Locate every Plasmodium parasite.
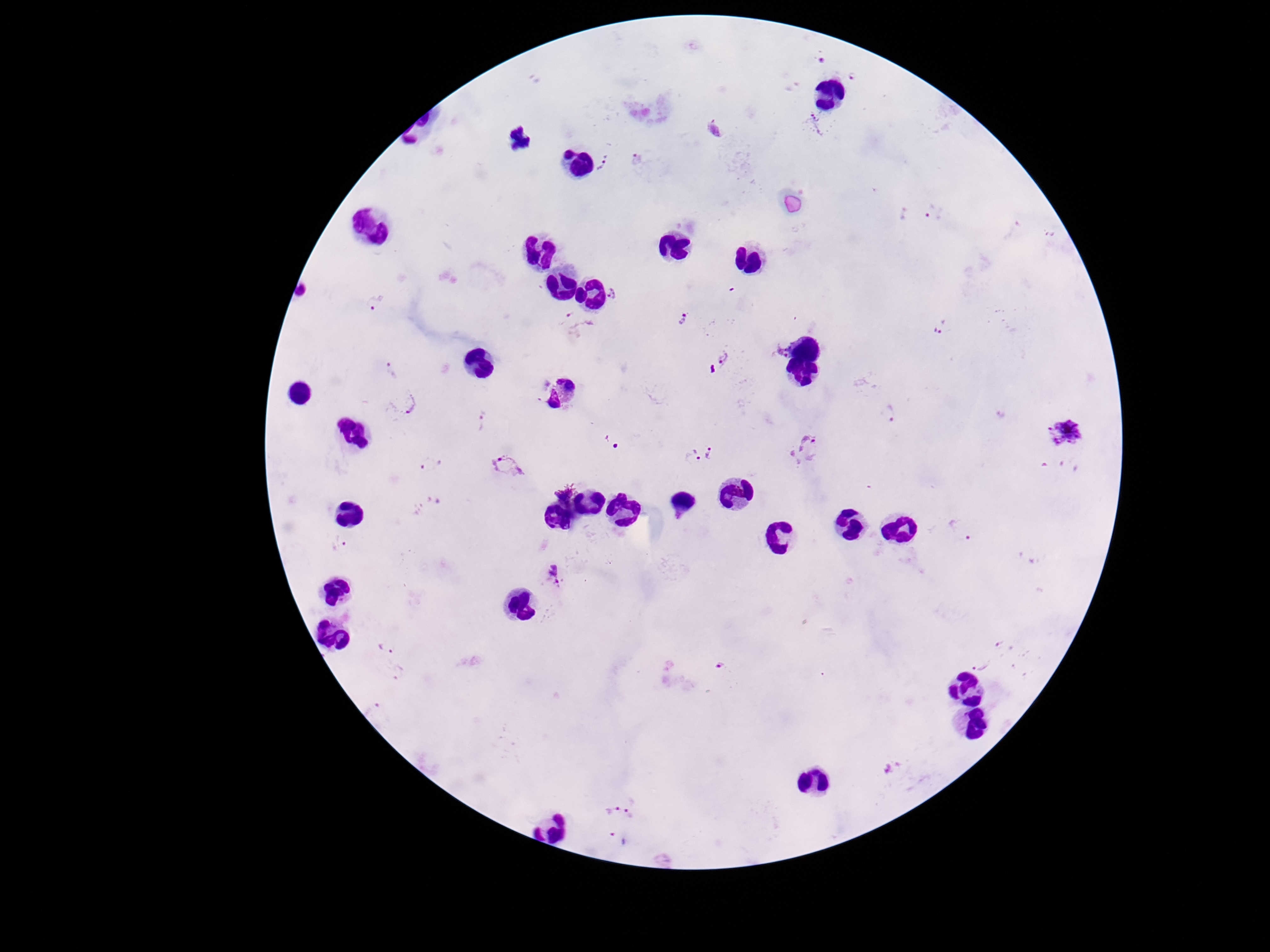

Approximate object centers, in pixels from the top-left corner.
Plasmodium parasites: (x=822, y=62), (x=853, y=76), (x=818, y=125), (x=638, y=159), (x=602, y=162), (x=920, y=215), (x=615, y=293), (x=375, y=305), (x=684, y=319), (x=579, y=326), (x=941, y=327), (x=781, y=349), (x=718, y=360), (x=390, y=372), (x=403, y=405), (x=889, y=414), (x=483, y=421), (x=1066, y=430), (x=613, y=443), (x=806, y=450), (x=716, y=454), (x=693, y=459), (x=430, y=465), (x=508, y=466), (x=428, y=506), (x=962, y=531), (x=341, y=544), (x=555, y=576), (x=1009, y=645), (x=386, y=648), (x=979, y=665), (x=722, y=666), (x=396, y=671), (x=372, y=708), (x=894, y=768), (x=637, y=809), (x=612, y=811), (x=618, y=840).

Summary:
  - Patient malaria status: positive
  - Preparation: thick blood smear
  - Image size: 1270×952 pixels
  - Stain: Giemsa
  - Magnification: 100x
  - Capture: smartphone camera through the microscope eyepiece
  - Field of view: one from this slide